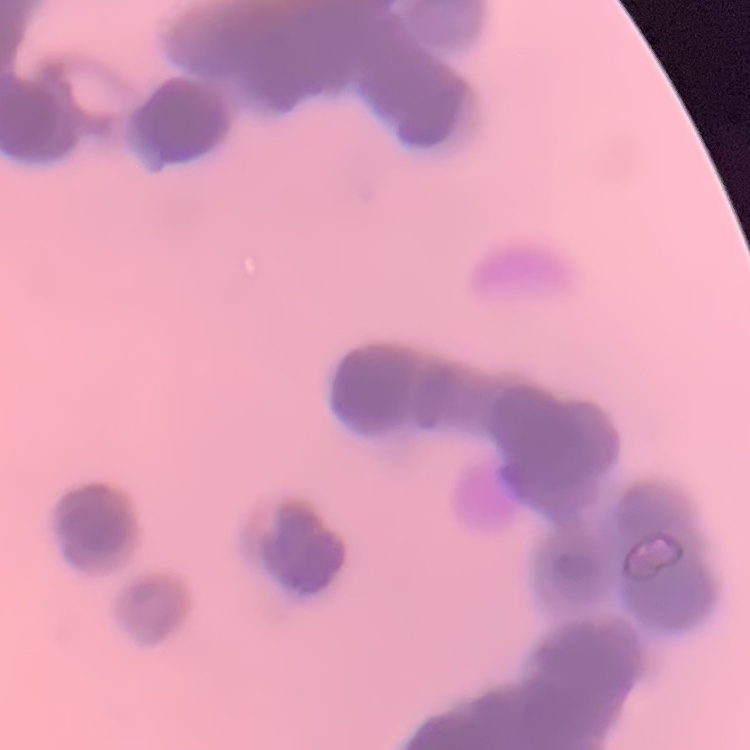
erythrocyte morphology = rouleaux formation
image type = square crop of a larger photomicrograph
stain = Field's or Giemsa
preparation = thin blood film